Assess the morphology of the red blood cells.
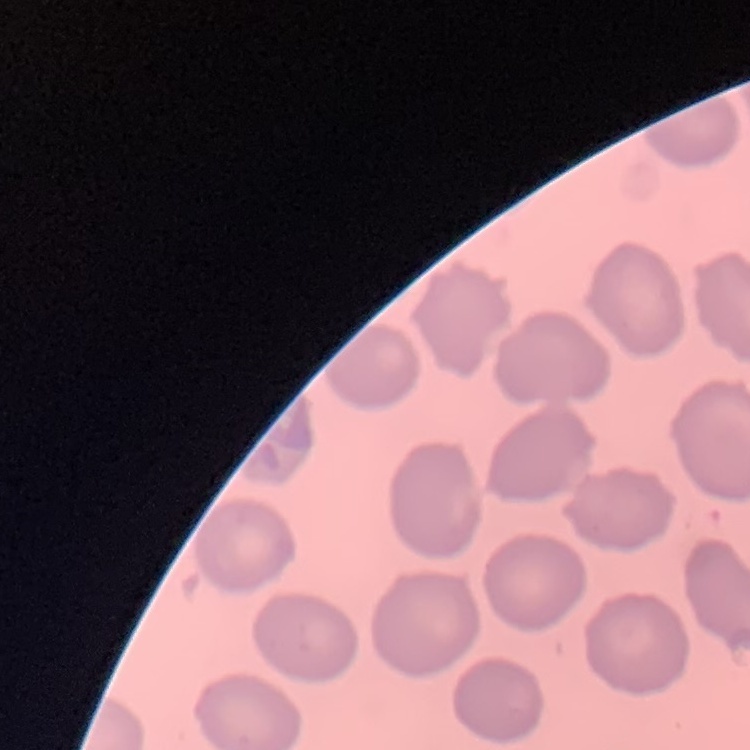
They show no rouleaux formation.

Summary:
  - Stain: Field's or Giemsa
  - Preparation: thin peripheral smear
  - Image type: one tile cut from a larger photomicrograph